Give the extent of all Plasmodium vivax-infected red blood cells.
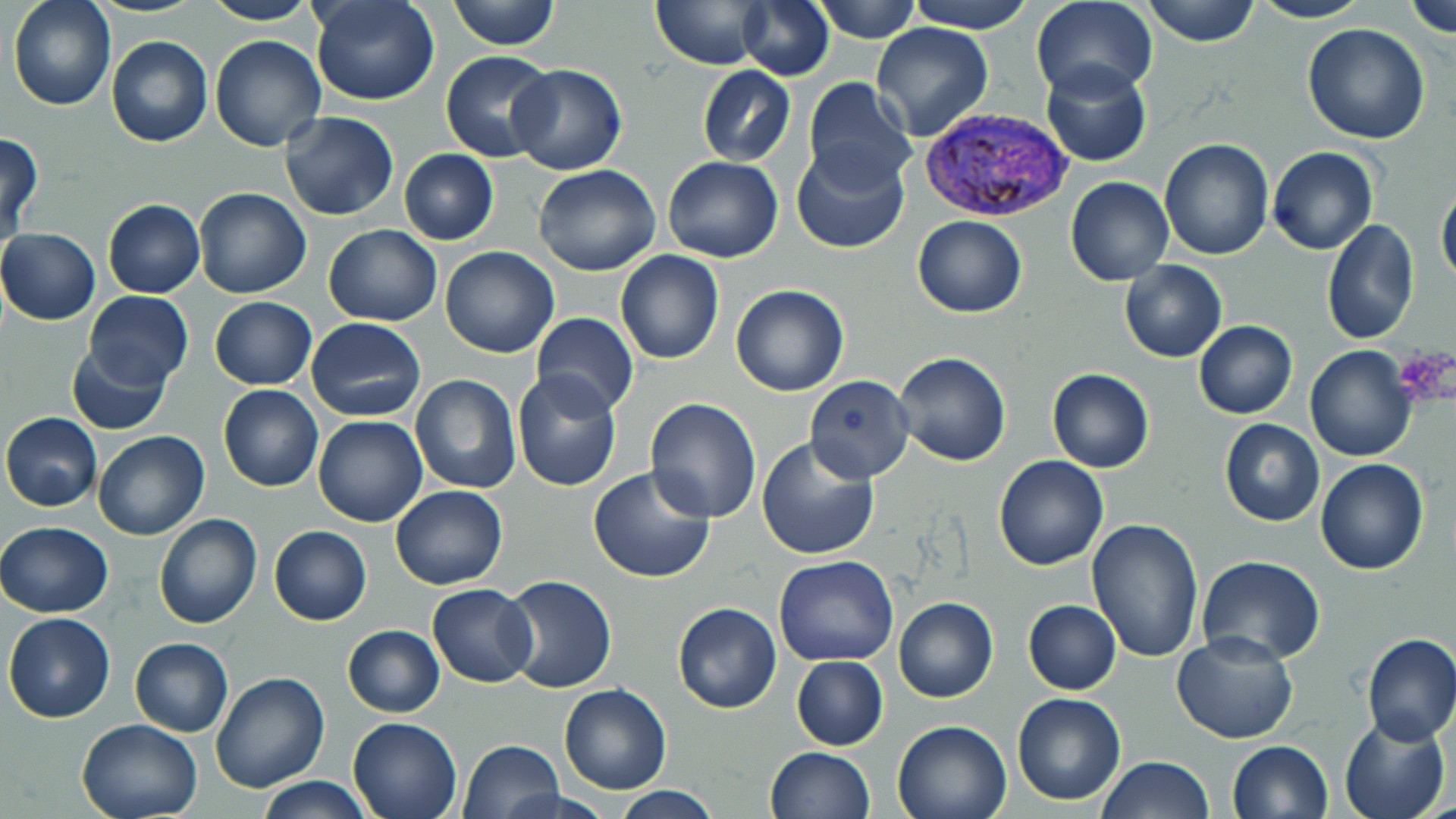
Approximate bounding boxes as (x1,y1)-(x2,y2) corner pairs in pixels.
Plasmodium vivax-infected red blood cells: (918,108)-(1073,225).

Summary:
  - Uninfected red blood cell locations: (7,0)-(115,111), (311,0)-(439,106), (448,0)-(560,50), (737,0)-(834,82), (813,0)-(920,41), (909,0)-(1034,34), (1143,0)-(1260,46), (1249,0)-(1373,23), (1405,0)-(1456,37), (202,1)-(320,26), (649,1)-(768,69), (1030,1)-(1158,100), (870,21)-(993,141), (1302,22)-(1431,144), (210,35)-(327,152), (106,36)-(213,147), (440,49)-(555,162), (1040,61)-(1151,167), (506,64)-(627,174), (696,66)-(796,166), (802,77)-(916,193), (280,110)-(399,221), (0,130)-(43,244), (1159,137)-(1273,259), (790,143)-(910,255), (1268,146)-(1378,255), (399,149)-(499,245), (662,156)-(783,263), (533,163)-(660,276), (1066,177)-(1174,286), (1437,183)-(1456,288), (192,187)-(311,298), (103,199)-(205,298), (912,215)-(1026,317), (1323,220)-(1418,346), (322,224)-(442,326), (0,228)-(101,324), (441,246)-(560,359), (615,250)-(724,364), (1119,259)-(1227,362), (731,284)-(850,397), (84,290)-(193,392), (208,296)-(318,390), (530,312)-(639,415), (306,317)-(426,421), (1194,320)-(1297,419), (67,343)-(170,434), (1305,346)-(1416,461), (893,350)-(1012,465), (1047,368)-(1153,473), (511,370)-(623,491), (410,374)-(521,493), (804,375)-(915,483), (218,384)-(323,492), (646,398)-(762,521), (1,412)-(103,512), (313,414)-(428,527), (1219,419)-(1324,526), (94,431)-(209,541), (757,437)-(881,561), (993,455)-(1108,571), (1315,458)-(1428,575), (587,466)-(716,584), (389,485)-(507,590), (153,513)-(262,628), (1087,518)-(1203,664), (1,521)-(113,617), (269,525)-(372,625), (773,554)-(899,666), (1196,555)-(1325,665), (498,575)-(618,693), (428,582)-(537,687), (894,597)-(998,703), (1023,599)-(1122,695), (671,603)-(782,714), (3,612)-(116,724), (342,624)-(445,717), (1361,632)-(1456,745), (1170,633)-(1298,744), (130,638)-(233,737), (791,655)-(887,751), (209,673)-(329,793), (558,684)-(671,795), (1012,692)-(1126,805), (348,716)-(462,819), (76,717)-(204,819), (1338,717)-(1450,819), (892,718)-(1013,819), (457,739)-(563,819), (1227,740)-(1334,819), (764,746)-(875,819), (1096,756)-(1215,819), (255,776)-(373,818), (611,787)-(721,818)
  - Platelet locations: (1392,347)-(1456,408)
  - Slide-level diagnosis: Plasmodium vivax
  - Modality: light microscopy
  - Magnification: 1000x
  - Image size: 1456×819 pixels
  - Preparation: thin blood smear
  - Field of view: single
  - Stain: May-Grünwald-Giemsa